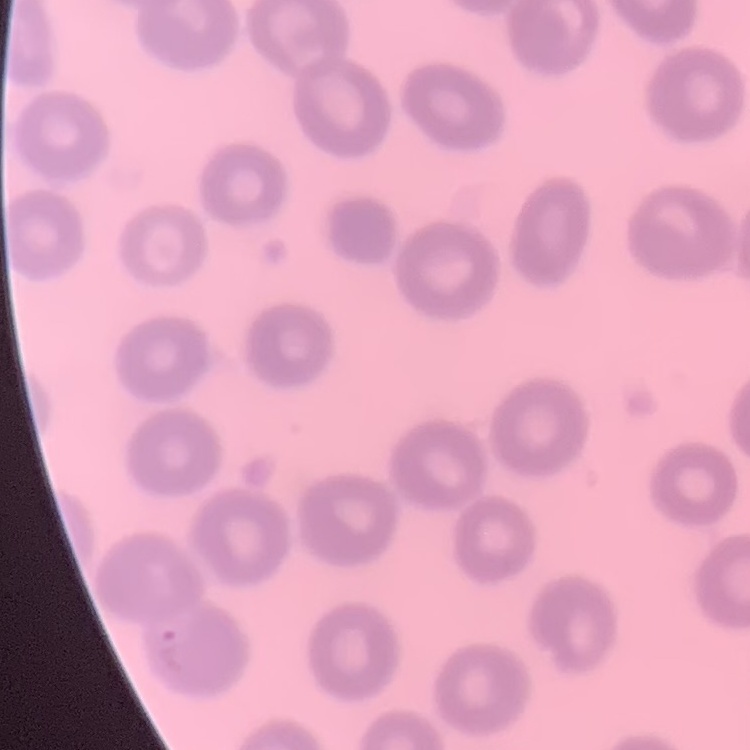
erythrocyte morphology = no rouleaux formation
preparation = thin blood smear
stain = Field's or Giemsa
image type = square crop of a larger photomicrograph